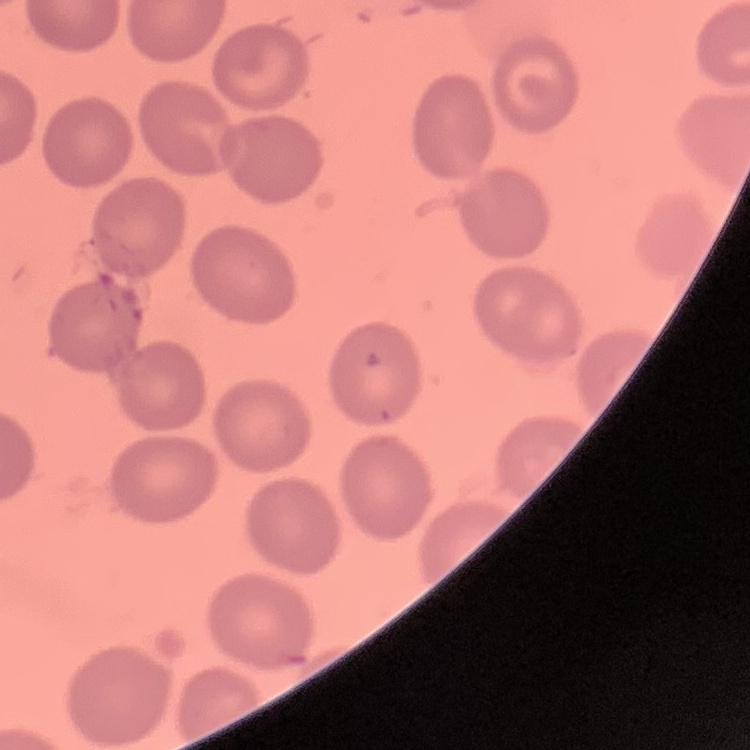
The red blood cells show no rouleaux formation. Field's or Giemsa stain. Thin blood smear. One tile cut from a larger photomicrograph.